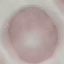

{
  "malaria_status": "uninfected",
  "preparation": "thin blood film",
  "stain": "Giemsa",
  "capture": "smartphone camera at the microscope eyepiece",
  "image_type": "automatically extracted cell patch, resized to 64 × 64 pixels"
}